Describe the morphology of the red blood cells.
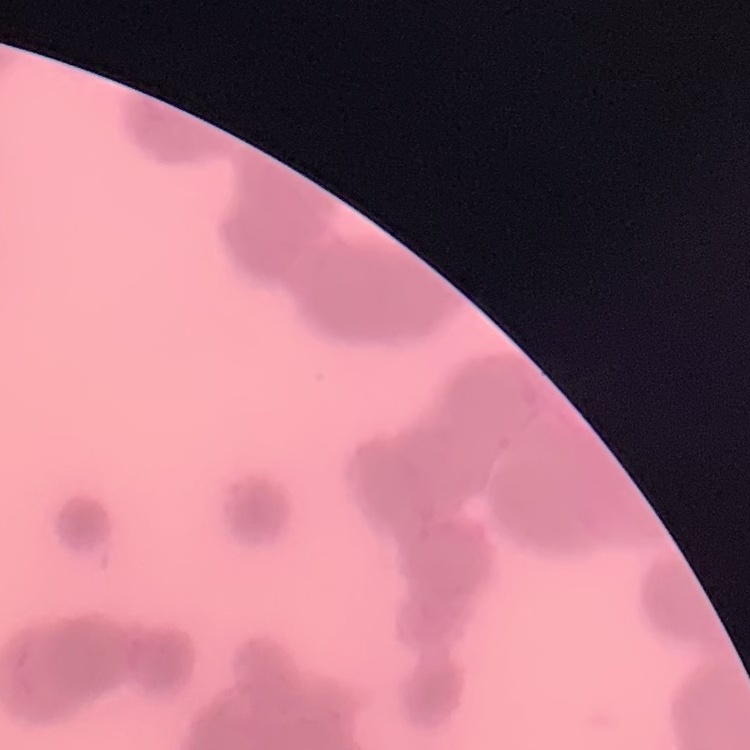

They show rouleaux formation.

Summary:
  - Image type: one tile cut from a larger photomicrograph
  - Stain: Field's or Giemsa
  - Preparation: thin blood smear